Identify the cell.
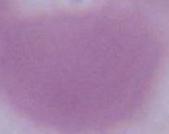
An erythrocyte.

{
  "magnification": "1000x",
  "modality": "photomicrograph"
}